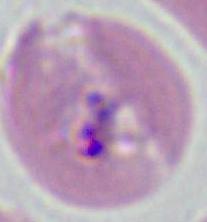

Photomicrograph. 400x or 1000x magnification. A Plasmodium parasite is shown.